Report the malaria status of this cell.
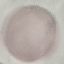

Uninfected.

Summary:
  - Stain: Giemsa
  - Capture: smartphone through the microscope eyepiece
  - Preparation: thin blood smear
  - Image type: automatically extracted cell patch, resized to 64 × 64 pixels